Describe the morphology of the erythrocytes.
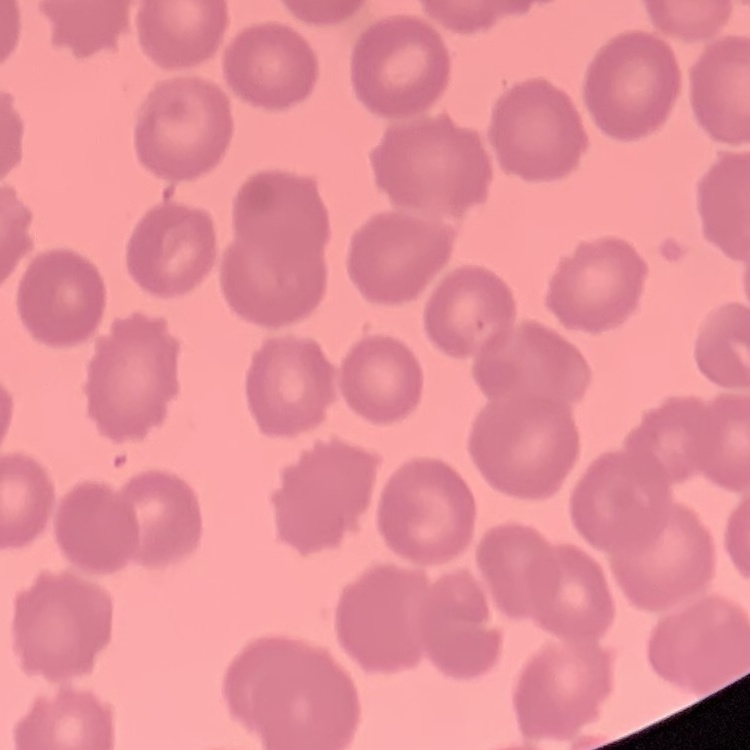

No rouleaux formation.

Summary:
  - Stain: Field's or Giemsa
  - Preparation: thin blood smear
  - Image type: one tile cut from a larger photomicrograph